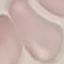
{
  "result": "negative for malaria parasites",
  "capture": "smartphone camera at the microscope eyepiece",
  "image_type": "cell patch, automatically extracted from a larger field of view and resized to 64 × 64 pixels",
  "stain": "Giemsa",
  "preparation": "thin smear"
}